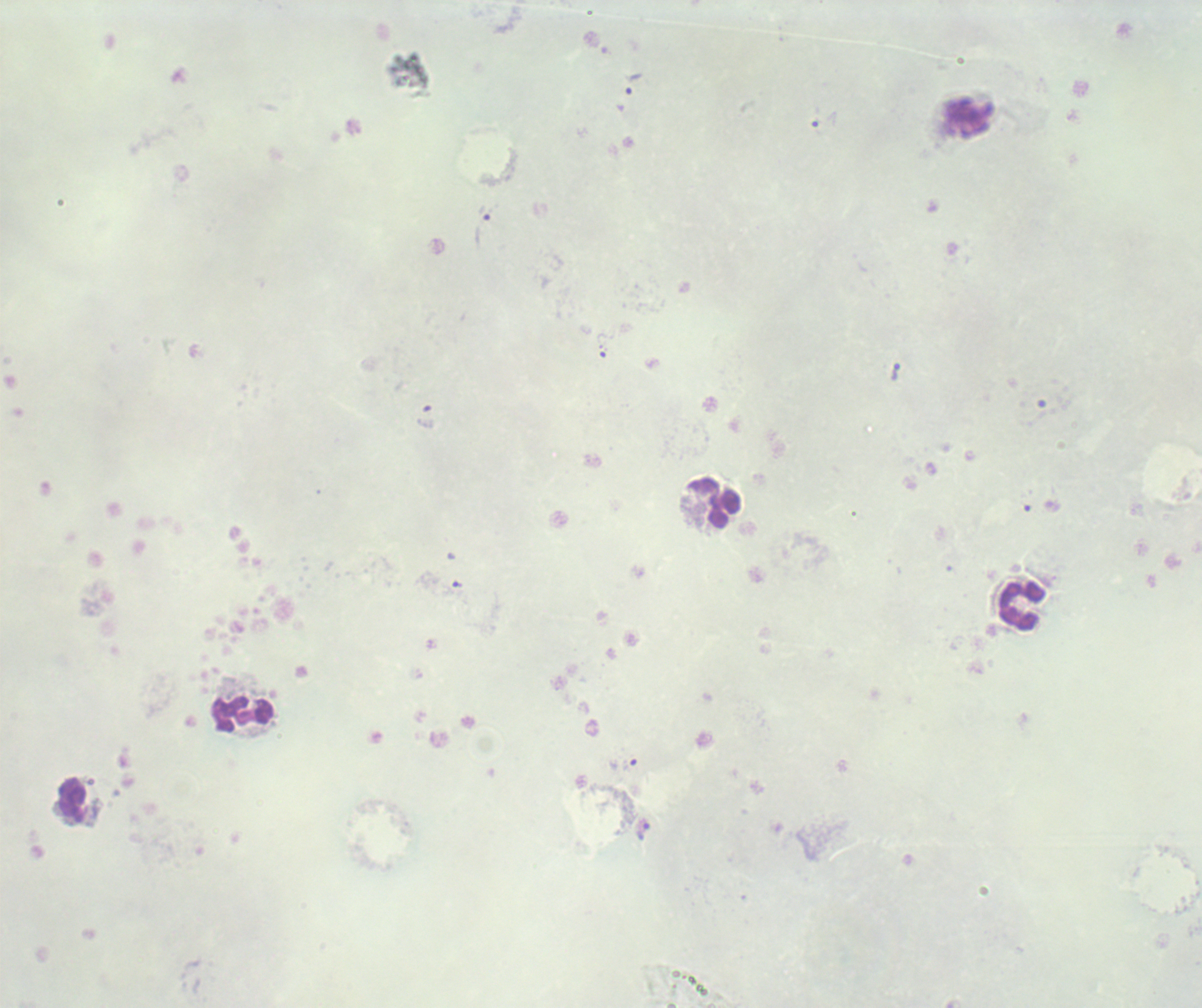 Approximate centers as {x, y} in pixels. Leukocyte locations: {714, 503}, {1022, 604}, {246, 715}, {72, 801}. Trophozoite locations: {633, 83}, {822, 119}, {488, 213}, {895, 371}, {642, 830}. Romanowsky-stained preparation. Thick smear of blood. Single field of view. 100x magnification. Coloration quality: bad. Background quality: unsatisfactory. Result: Plasmodium parasites identified. Image is 1202×1008 pixels. Previously used in a real diagnosis.